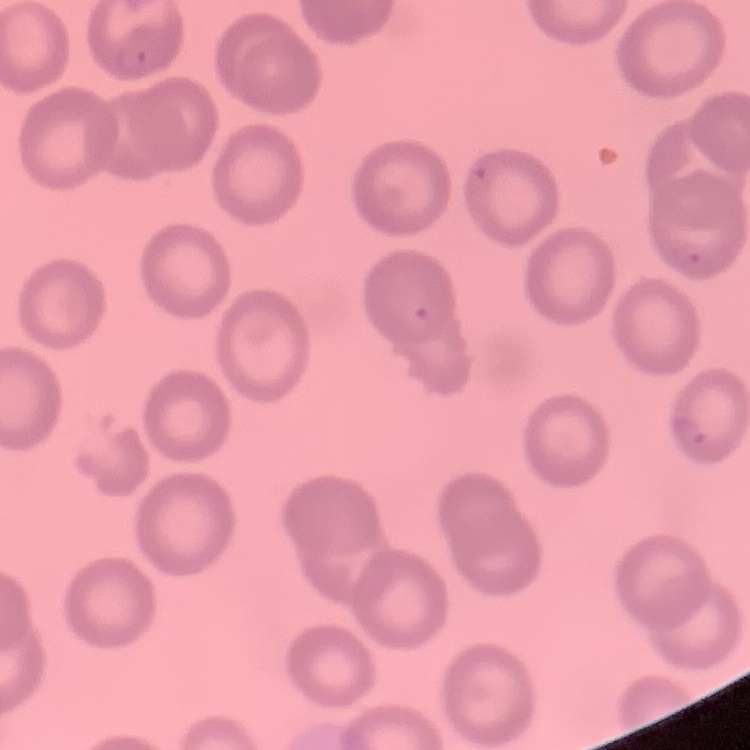
The erythrocytes show no rouleaux formation. Field's or Giemsa stain. Thin peripheral smear. One tile cut from a larger photomicrograph.